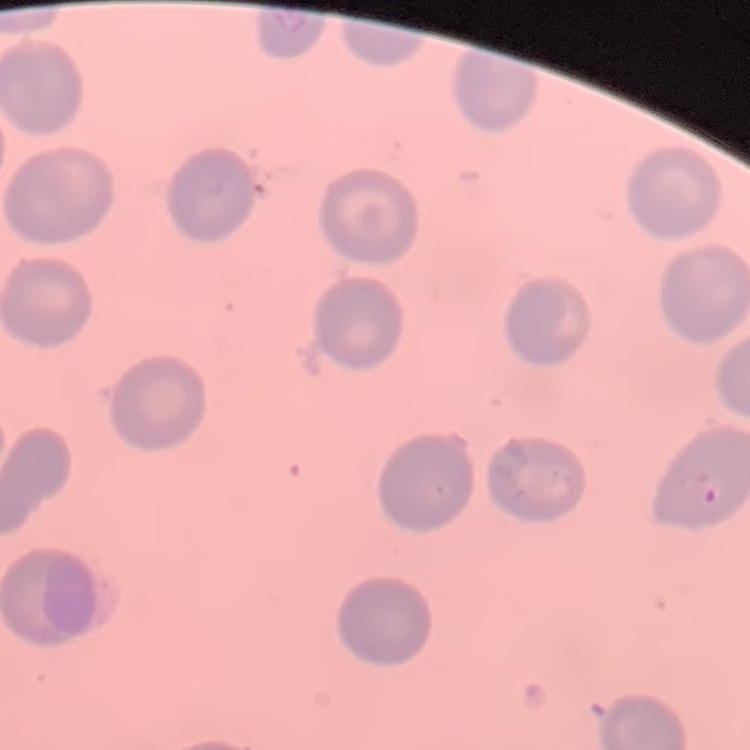 The red blood cells show no rouleaux formation. Square crop of a larger photomicrograph. Thin blood smear. Field's or Giemsa stain.